Comment on the morphology of the red blood cells.
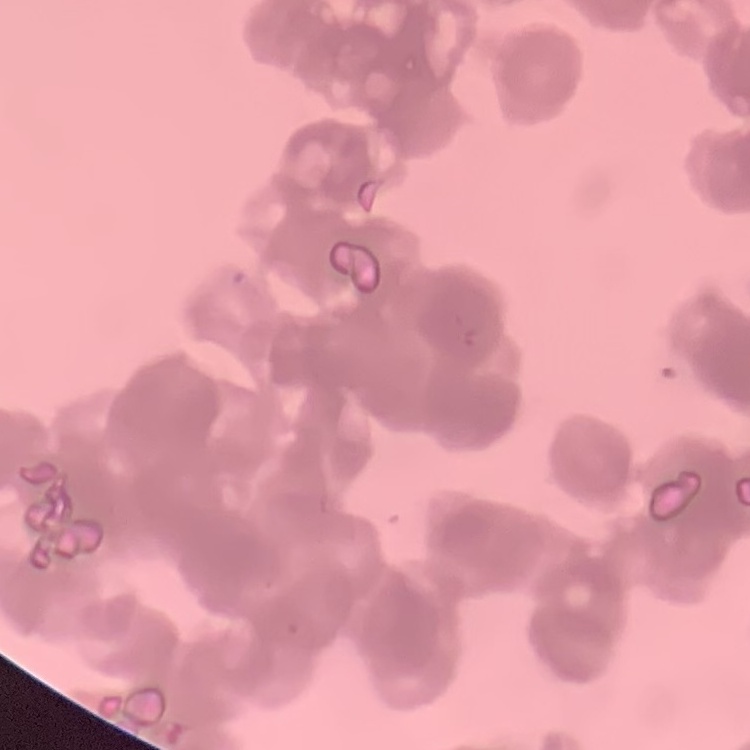

They show rouleaux formation.

Summary:
  - Stain: Field's or Giemsa
  - Image type: one tile cut from a larger photomicrograph
  - Preparation: thin peripheral smear